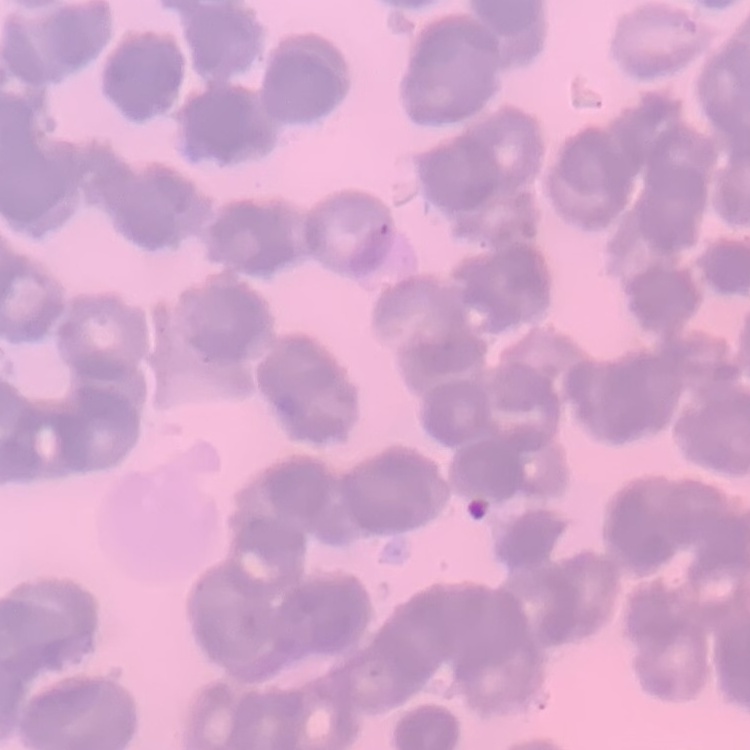
Summary:
  - Erythrocyte morphology: rouleaux formation
  - Image type: one tile cut from a larger photomicrograph
  - Stain: Field's or Giemsa
  - Preparation: thin blood smear